Report the malaria status of this cell.
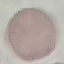

It is uninfected.

Summary:
  - Preparation: thin blood film
  - Image type: cell patch, automatically extracted from a larger field of view and resized to 64 × 64 pixels
  - Stain: Giemsa
  - Capture: smartphone camera at the microscope eyepiece